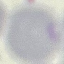
result = negative for malaria parasites
capture = smartphone camera at the microscope eyepiece
image type = automatically extracted cell patch, resized to 64 × 64 pixels
preparation = thin blood smear
stain = Giemsa